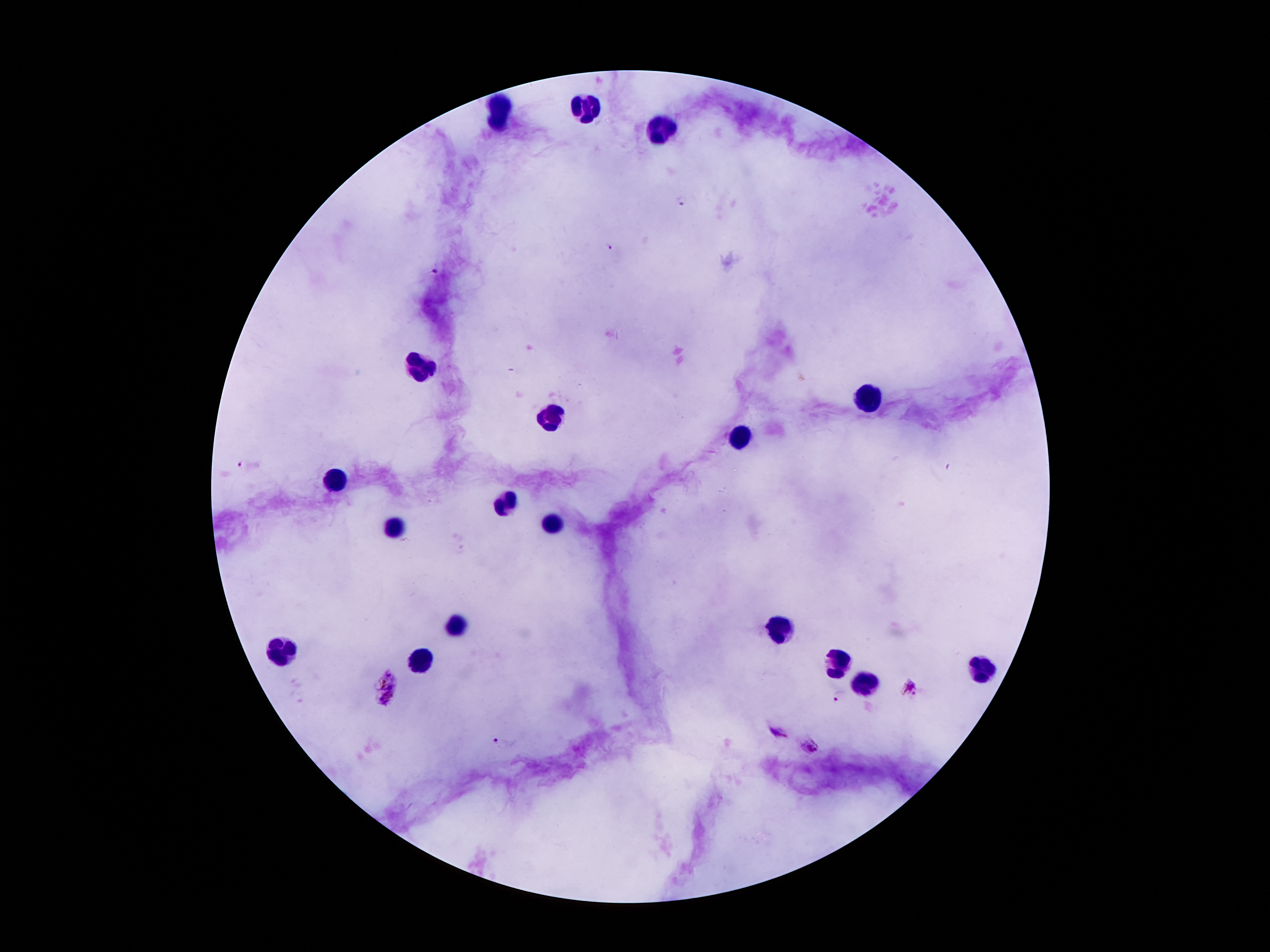

coordinate format = approximate centers as {x, y} in pixels
Plasmodium parasite locations = {682, 203}, {611, 246}, {435, 271}, {240, 463}, {385, 677}, {912, 687}, {840, 695}, {386, 701}, {777, 731}, {497, 741}, {811, 748}
leukocyte locations = {498, 102}, {585, 108}, {496, 125}, {665, 134}, {425, 367}, {868, 398}, {549, 416}, {739, 439}, {334, 479}, {506, 504}, {557, 524}, {394, 526}, {457, 629}, {779, 630}, {283, 650}, {423, 657}, {834, 666}, {983, 672}, {866, 683}
magnification = 100x
preparation = thick peripheral-blood smear
stain = Giemsa
image size = 1270×952 pixels
patient malaria status = positive for Plasmodium falciparum
field of view = one from this slide
capture = smartphone camera through the microscope eyepiece